Locate every Plasmodium ovale-infected red blood cell.
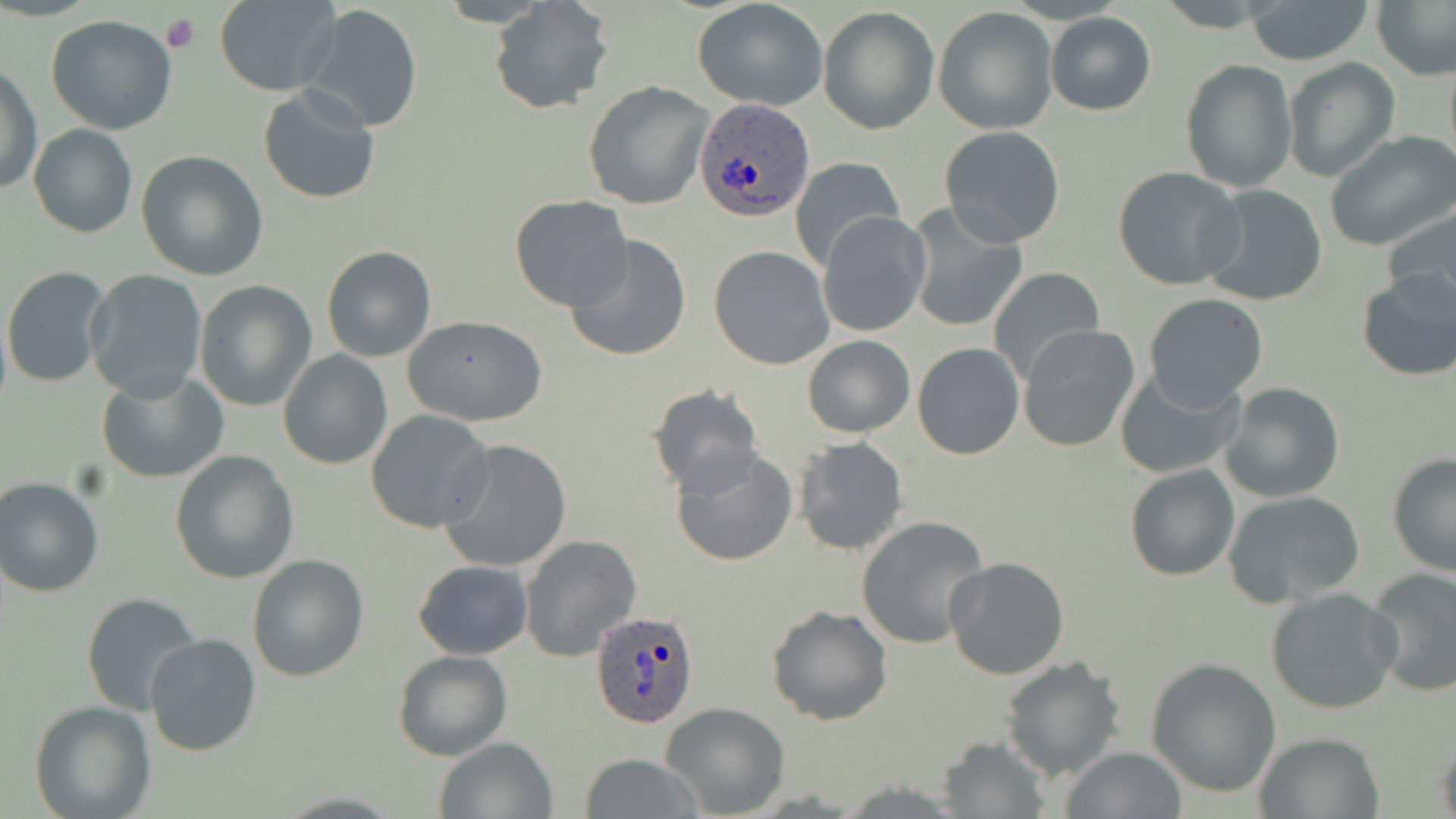
Approximate bounding boxes as [x1, y1, x2, y2] in pixels.
Plasmodium ovale-infected red blood cells: [696, 99, 816, 224], [591, 610, 700, 730].

Summary:
  - Uninfected red blood cell locations: [487, 0, 614, 116], [692, 0, 830, 110], [1154, 0, 1285, 31], [1240, 0, 1376, 65], [213, 1, 341, 95], [1374, 2, 1456, 79], [298, 4, 423, 133], [818, 6, 940, 135], [932, 7, 1058, 135], [1045, 13, 1156, 114], [45, 16, 179, 135], [1443, 52, 1456, 173], [1281, 57, 1401, 184], [1180, 58, 1296, 193], [2, 62, 41, 198], [584, 80, 713, 209], [257, 85, 382, 204], [28, 122, 137, 239], [938, 126, 1067, 249], [1324, 130, 1456, 252], [137, 151, 268, 281], [789, 157, 907, 271], [1112, 165, 1246, 290], [1199, 183, 1329, 307], [510, 196, 635, 311], [1380, 201, 1456, 313], [905, 204, 1028, 333], [816, 211, 931, 337], [564, 233, 693, 361], [322, 245, 436, 362], [708, 245, 835, 370], [2, 265, 113, 389], [1354, 265, 1456, 380], [989, 266, 1107, 384], [84, 267, 209, 401], [194, 280, 317, 411], [1142, 293, 1270, 412], [402, 314, 547, 426], [1017, 325, 1141, 453], [802, 335, 914, 437], [912, 343, 1025, 459], [278, 351, 393, 471], [1115, 366, 1246, 480], [96, 371, 227, 484], [1217, 380, 1347, 503], [645, 384, 765, 497], [365, 409, 493, 533], [792, 435, 909, 557], [437, 438, 573, 574], [670, 445, 799, 567], [170, 451, 298, 584], [1387, 453, 1456, 577], [1125, 464, 1240, 582], [0, 475, 104, 597], [1222, 489, 1366, 608], [856, 516, 990, 649], [518, 533, 642, 662], [247, 555, 370, 682], [944, 558, 1070, 681], [413, 559, 532, 660], [1365, 568, 1456, 697], [1266, 587, 1403, 715], [80, 592, 202, 718], [766, 605, 893, 726], [144, 634, 263, 757], [393, 650, 510, 760], [1000, 655, 1126, 781], [1147, 658, 1281, 797], [29, 701, 155, 819], [659, 701, 789, 817], [1254, 731, 1385, 818], [936, 734, 1052, 817], [1436, 734, 1456, 819], [434, 737, 557, 818], [1061, 746, 1186, 818], [577, 753, 704, 819]
  - Platelet locations: [160, 12, 201, 53]
  - Slide-level diagnosis: Plasmodium ovale
  - Preparation: thin blood smear
  - Modality: light microscopy
  - Field of view: single
  - Stain: May-Grünwald-Giemsa
  - Image size: 1456×819 pixels
  - Magnification: 1000x